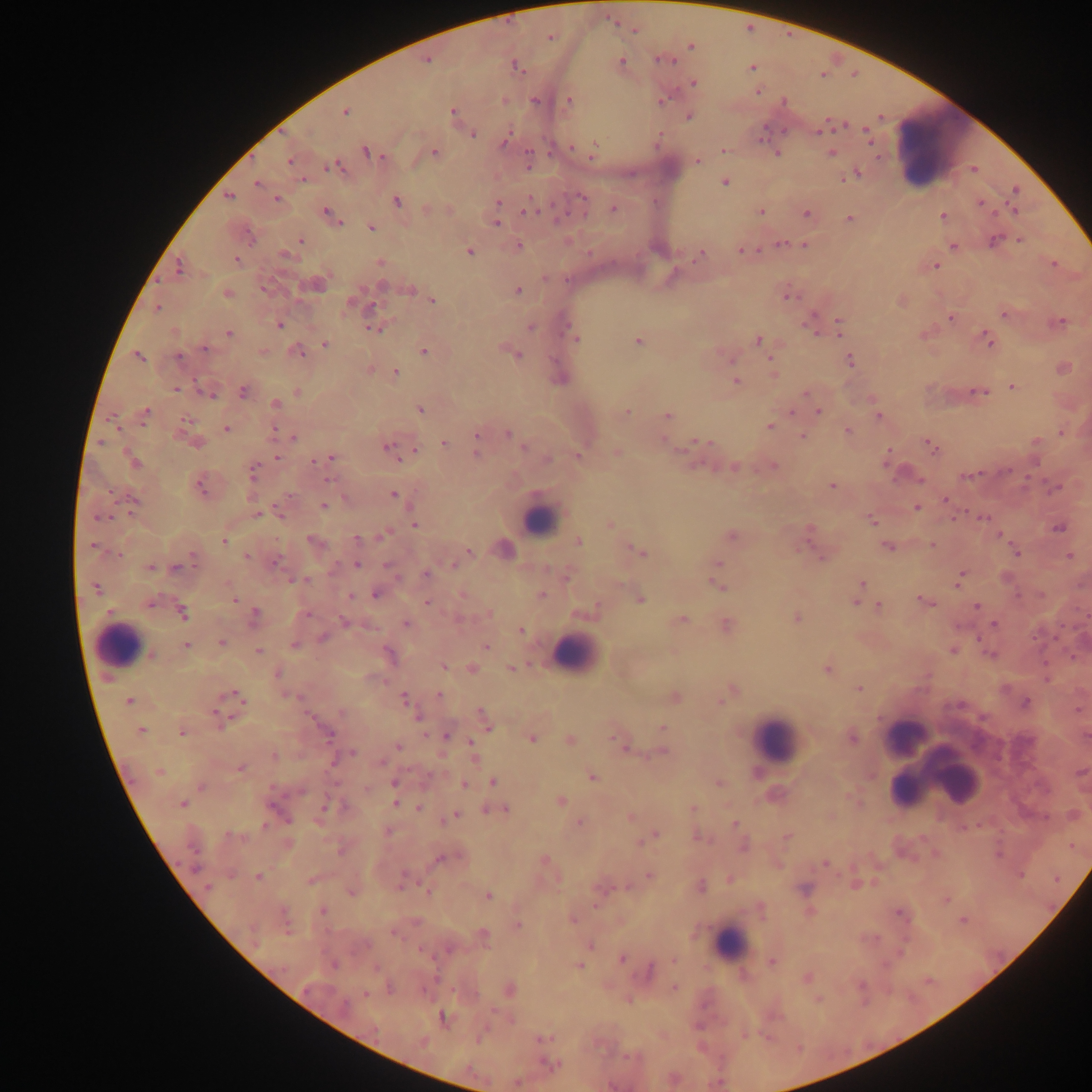

Approximate centers as x y in pixels.
Summary:
  - Malaria parasite locations: 614 23; 635 31; 549 38; 656 59; 621 60; 672 61; 514 65; 753 69; 758 92; 569 100; 534 101; 503 102; 454 111; 345 113; 866 128; 817 133; 866 133; 474 134; 506 138; 762 139; 596 142; 870 142; 571 146; 724 151; 365 152; 527 152; 433 153; 778 153; 830 153; 877 157; 592 159; 289 160; 699 160; 334 163; 325 167; 858 172; 301 179; 842 179; 726 182; 258 183; 529 195; 229 196; 276 199; 396 200; 498 200; 978 201; 1005 202; 612 209; 760 211; 326 212; 1013 212; 523 214; 541 214; 806 214; 942 215; 993 215; 851 219; 497 223; 342 224; 372 227; 301 240; 992 240; 1017 241; 780 243; 804 244; 952 245; 519 246; 758 250; 740 251; 470 252; 236 258; 1054 264; 936 266; 179 269; 544 279; 412 290; 518 290; 786 296; 353 299; 433 301; 157 308; 1003 313; 950 317; 837 318; 1061 321; 1050 322; 279 324; 374 328; 528 328; 984 330; 988 330; 229 332; 816 333; 840 335; 577 338; 757 339; 637 340; 324 344; 992 345; 204 347; 301 350; 424 352; 519 356; 139 357; 179 357; 730 359; 770 359; 850 360; 395 372; 735 380; 1013 387; 176 391; 970 391; 978 391; 242 392; 805 392; 986 392; 200 393; 212 395; 274 404; 420 409; 146 412; 628 412; 819 412; 792 413; 668 415; 110 416; 879 417; 185 420; 769 427; 117 428; 227 428; 275 428; 847 431; 1060 433; 801 434; 512 436; 293 438; 663 439; 1035 440; 925 442; 101 443; 443 443; 476 443; 690 444; 931 444; 387 446; 523 447; 414 449; 888 449; 391 451; 934 453; 277 457; 320 460; 399 460; 548 460; 1036 460; 885 463; 734 467; 772 467; 1010 469; 252 470; 976 475; 966 476; 322 478; 920 480; 1041 480; 832 486; 1024 486; 1057 488; 392 495; 945 502; 324 506; 918 508; 964 508; 256 513; 129 514; 113 515; 98 517; 981 517; 951 518; 873 521; 415 525; 1057 528; 809 529; 388 532; 999 535; 358 539; 223 542; 933 543; 92 545; 887 547; 469 550; 1017 554; 120 555; 1069 555; 247 556; 822 556; 193 558; 278 560; 717 563; 453 564; 358 565; 385 565; 150 568; 176 568; 425 574; 398 578; 307 580; 711 581; 960 582; 863 584; 97 588; 374 594; 462 596; 1018 596; 1041 596; 350 597; 919 597; 235 599; 153 601; 427 603; 855 603; 151 604; 867 604; 878 605; 933 605; 977 606; 255 611; 183 613; 488 614; 306 615; 796 617; 682 620; 342 621; 405 623; 1061 623; 995 625; 522 631; 321 637; 1033 637; 978 639; 1055 639; 221 643; 186 645; 486 647; 952 650; 257 651; 989 653; 1045 662; 444 666; 510 667; 827 669; 1046 678; 859 688; 440 695; 221 698; 403 698; 240 699; 720 702; 1026 702; 960 706; 341 713; 233 718; 219 726; 662 727; 182 733; 329 734; 445 735; 852 737; 613 739; 469 740; 532 740; 619 743; 398 747; 661 751; 352 754; 275 756; 382 762; 239 769; 592 776; 393 782; 494 783; 719 783; 465 785; 201 787; 272 789; 366 789; 184 801; 561 801; 395 802; 324 807; 419 807; 691 809; 456 814; 1043 817; 579 822; 735 823; 263 826; 962 828; 228 835; 696 836; 786 837; 923 839; 645 841; 341 852; 935 854; 544 860; 823 863; 196 868; 648 875; 1019 876; 257 877; 854 884; 208 886; 400 887; 424 888; 351 892; 427 892; 486 896; 946 898; 896 910; 323 911; 962 919; 518 924; 392 933; 876 939; 621 959; 673 959; 772 962; 580 965; 375 966; 650 969; 807 979; 673 988; 425 991; 364 994; 818 999; 745 1035; 541 1039; 798 1048
  - Leukocyte locations: 934 150; 540 522; 578 648; 123 650; 776 738; 932 762; 727 949
  - Capture: mobile-phone photograph through a microscope
  - Country: Ghana
  - Image size: 1092×1092 pixels
  - Preparation: thick blood film
  - Field of view: single